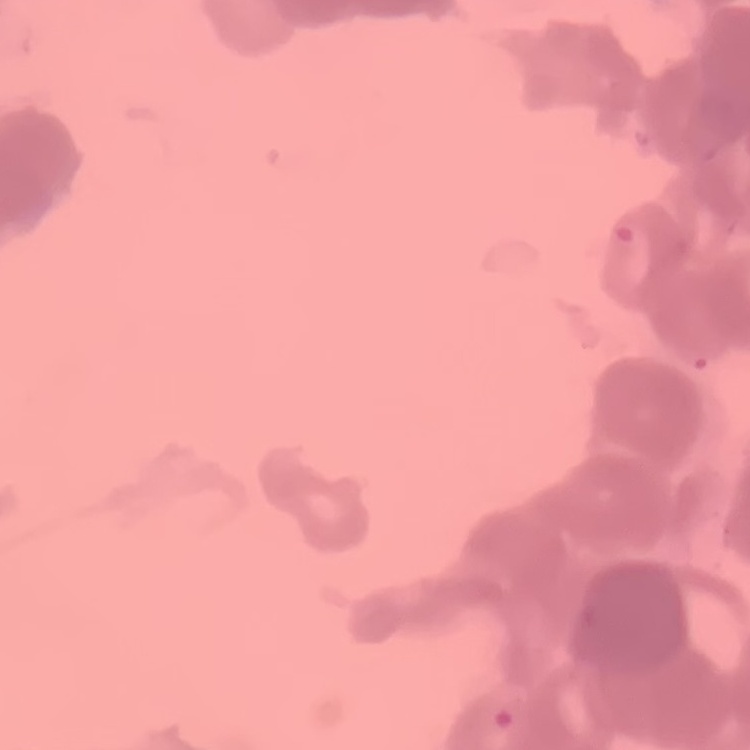 The erythrocytes exhibit rouleaux formation. Stained with either Field's or Giemsa. Thin blood smear. One tile cut from a larger photomicrograph.